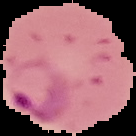
The area outside the segmented cell region is set to black. From a thin blood film. Result: Plasmodium parasites detected. Image is 136×136 pixels.